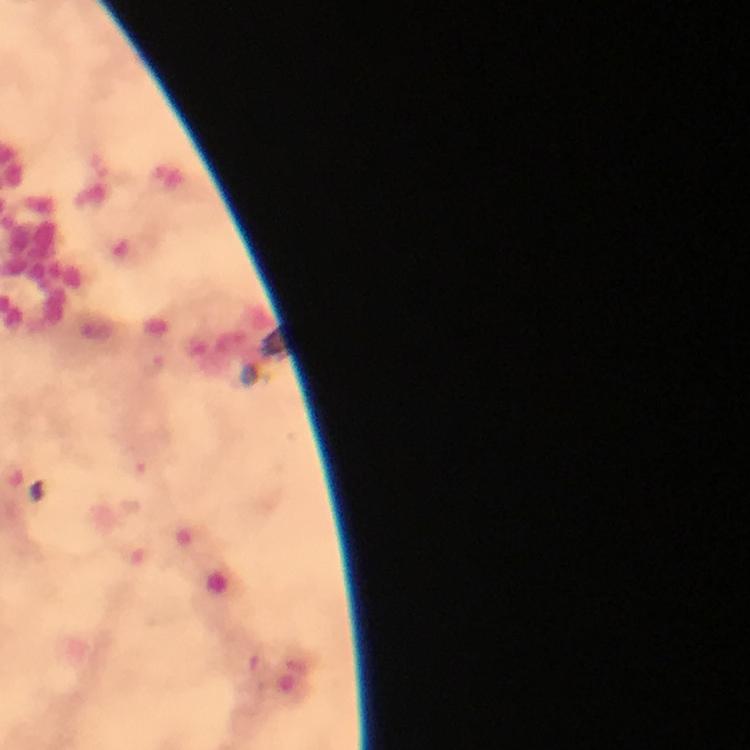

Approximate centers as [x, y] in pixels.
Summary:
  - Plasmodium parasite locations: [153, 363]
  - Context: from a malaria diagnostic workup
  - Capture: smartphone mounted on the microscope
  - Stain: Giemsa
  - Immersion oil: applied
  - Image size: 750×750 pixels
  - Preparation: thick blood film
  - Magnification: 100x
  - Cropped from: a single field of view